Report the malaria status of this cell.
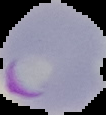
Parasitized.

image type = segmented cell region with the area outside set to black
preparation = thin blood film
image size = 106×115 pixels